Outline each blood parasite and name the species.
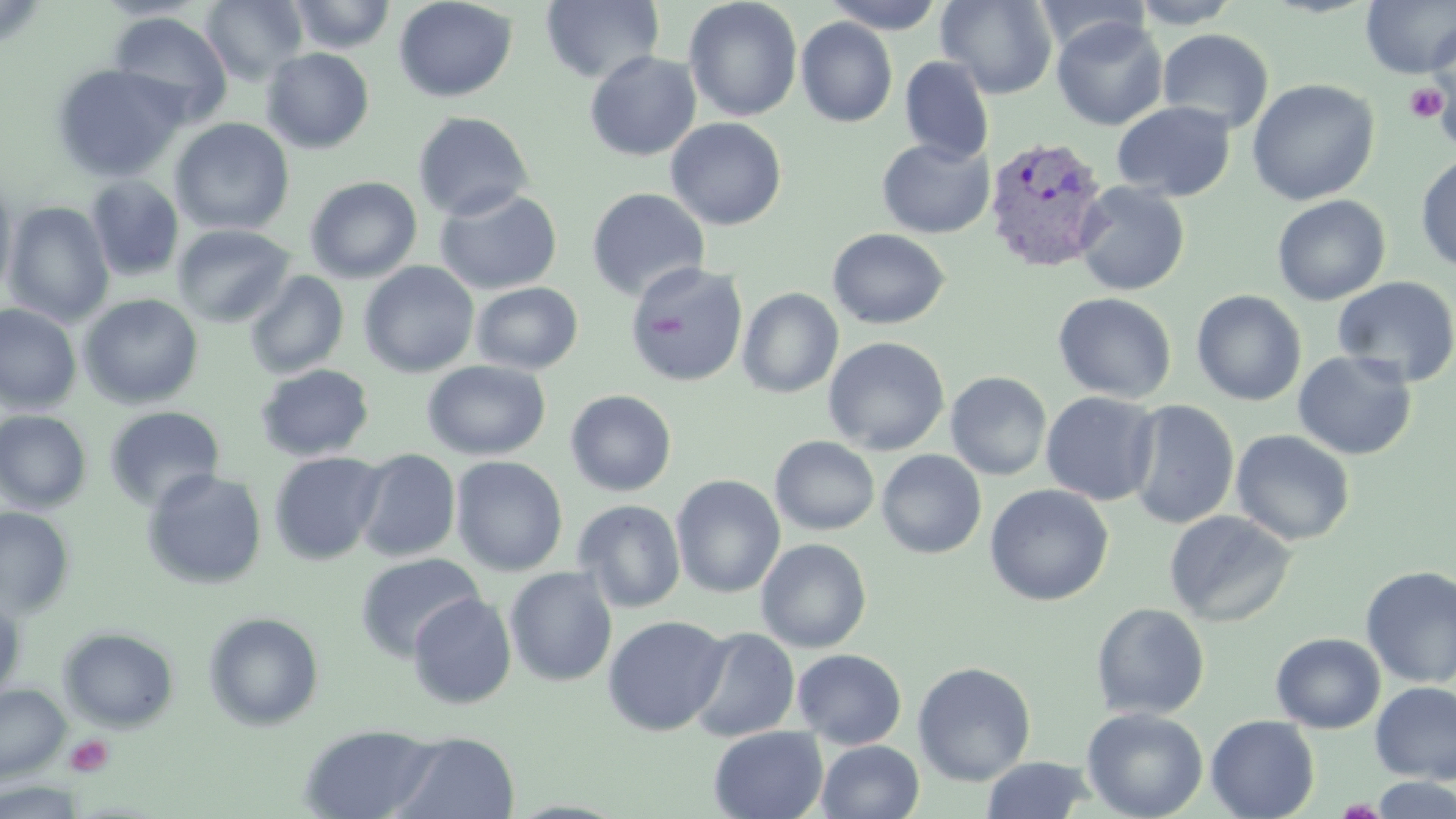

Approximate bounding boxes as [x1, y1, x2, y2] in pixels.
Plasmodium vivax-infected red blood cells: [983, 136, 1111, 274].
No Plasmodium falciparum, Plasmodium ovale, Plasmodium malariae, Babesia divergens, or Trypanosoma brucei observed.

Platelet locations: [1404, 82, 1449, 124], [66, 734, 113, 776]. Uninfected red blood cell locations: [200, 0, 308, 84], [286, 0, 397, 54], [393, 0, 517, 102], [541, 0, 664, 84], [823, 0, 944, 33], [936, 0, 1057, 99], [1034, 0, 1151, 57], [1129, 0, 1242, 28], [1360, 0, 1456, 79], [683, 1, 802, 122], [106, 11, 234, 126], [1051, 16, 1168, 131], [795, 17, 898, 127], [1425, 21, 1456, 136], [1157, 29, 1274, 134], [261, 47, 375, 154], [584, 51, 702, 161], [899, 56, 994, 165], [51, 62, 189, 183], [1246, 78, 1380, 206], [1112, 101, 1236, 201], [412, 111, 534, 222], [170, 117, 295, 236], [666, 117, 787, 230], [876, 138, 995, 238], [1415, 153, 1456, 273], [0, 174, 17, 303], [85, 175, 185, 282], [304, 176, 422, 283], [1074, 182, 1191, 296], [586, 187, 709, 302], [434, 188, 562, 295], [1272, 195, 1391, 306], [3, 201, 114, 327], [172, 223, 295, 329], [827, 228, 950, 330], [358, 261, 480, 378], [625, 261, 749, 387], [243, 270, 349, 379], [1332, 276, 1456, 388], [470, 282, 584, 374], [737, 288, 844, 398], [1191, 290, 1307, 406], [1053, 292, 1177, 403], [79, 294, 204, 409], [0, 304, 82, 414], [822, 336, 950, 455], [1292, 350, 1418, 460], [422, 360, 551, 460], [254, 363, 375, 462], [945, 371, 1052, 480], [565, 389, 678, 496], [1041, 391, 1161, 506], [1125, 400, 1239, 529], [103, 405, 225, 512], [0, 410, 93, 513], [1230, 429, 1355, 546], [770, 435, 880, 536], [353, 448, 461, 562], [877, 450, 987, 559], [268, 451, 388, 566], [450, 455, 568, 576], [141, 469, 268, 590], [671, 474, 785, 598], [984, 484, 1114, 606], [572, 499, 686, 613], [0, 506, 75, 619], [1163, 510, 1296, 627], [755, 538, 872, 653], [355, 552, 485, 663], [1359, 565, 1456, 689], [505, 566, 618, 687], [406, 592, 517, 709], [0, 595, 25, 703], [1091, 602, 1210, 720], [202, 611, 325, 731], [602, 615, 730, 736], [58, 626, 180, 733], [687, 626, 801, 743], [1270, 632, 1385, 733], [792, 649, 907, 749], [912, 661, 1036, 785], [1370, 681, 1456, 784], [0, 684, 70, 782], [1082, 707, 1208, 819], [1205, 715, 1320, 819], [299, 724, 440, 819], [709, 725, 829, 819], [390, 731, 520, 819], [816, 740, 925, 819], [981, 756, 1095, 818], [1369, 775, 1456, 818], [0, 780, 87, 818]. Slide-level diagnosis: Plasmodium vivax. Image is 1456×819 pixels. Captured at 1000x magnification. Light microscopy. May-Grünwald-Giemsa stain. Single field of view. Thin blood smear.